Outline each blood parasite and name the species.
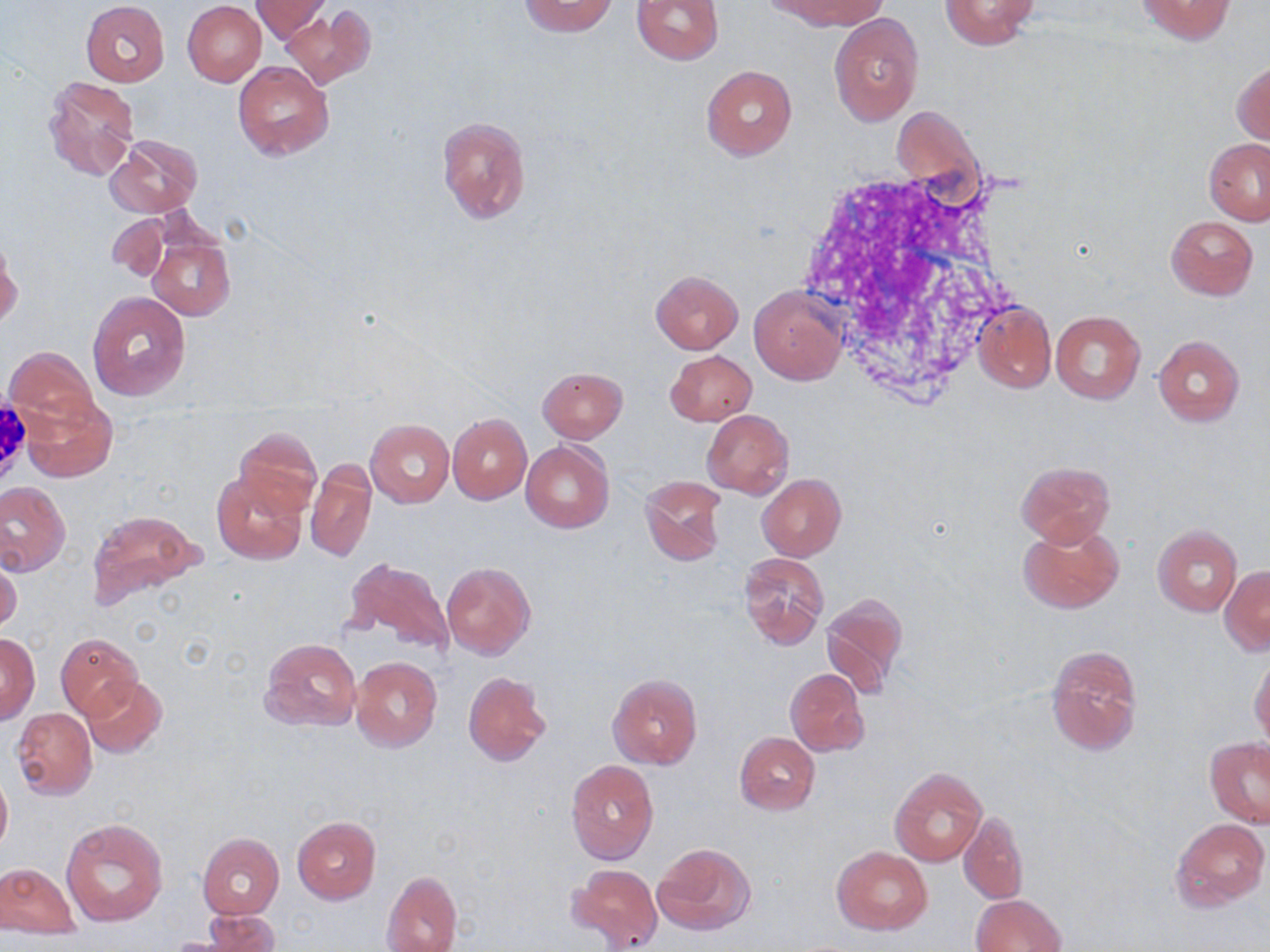

No blood parasites seen.

Approximate bounding boxes as named x1/y1/x2/y2 corners in pixels. Uninfected red blood cell locations: (x1=252, y1=0, x2=330, y2=43), (x1=518, y1=0, x2=617, y2=36), (x1=632, y1=0, x2=725, y2=65), (x1=772, y1=0, x2=885, y2=30), (x1=1133, y1=0, x2=1236, y2=44), (x1=81, y1=1, x2=169, y2=86), (x1=183, y1=1, x2=266, y2=86), (x1=938, y1=1, x2=1041, y2=49), (x1=281, y1=5, x2=375, y2=89), (x1=830, y1=13, x2=923, y2=125), (x1=1232, y1=60, x2=1270, y2=146), (x1=232, y1=61, x2=333, y2=161), (x1=701, y1=65, x2=795, y2=160), (x1=43, y1=75, x2=139, y2=183), (x1=436, y1=114, x2=531, y2=224), (x1=105, y1=134, x2=203, y2=220), (x1=1204, y1=138, x2=1270, y2=225), (x1=107, y1=214, x2=169, y2=281), (x1=1166, y1=215, x2=1258, y2=300), (x1=146, y1=228, x2=235, y2=321), (x1=1, y1=240, x2=21, y2=329), (x1=650, y1=270, x2=744, y2=353), (x1=750, y1=286, x2=846, y2=385), (x1=85, y1=290, x2=191, y2=401), (x1=973, y1=302, x2=1055, y2=393), (x1=1051, y1=310, x2=1145, y2=405), (x1=1153, y1=335, x2=1245, y2=426), (x1=4, y1=346, x2=102, y2=433), (x1=665, y1=350, x2=756, y2=425), (x1=536, y1=366, x2=628, y2=443), (x1=20, y1=390, x2=117, y2=482), (x1=702, y1=409, x2=794, y2=499), (x1=447, y1=413, x2=532, y2=504), (x1=365, y1=419, x2=454, y2=507), (x1=232, y1=427, x2=323, y2=519), (x1=521, y1=440, x2=615, y2=534), (x1=306, y1=459, x2=377, y2=564), (x1=1016, y1=460, x2=1116, y2=546), (x1=210, y1=470, x2=308, y2=565), (x1=756, y1=474, x2=846, y2=562), (x1=640, y1=475, x2=727, y2=566), (x1=0, y1=481, x2=71, y2=575), (x1=87, y1=510, x2=203, y2=610), (x1=1018, y1=520, x2=1124, y2=614), (x1=1152, y1=525, x2=1241, y2=616), (x1=738, y1=552, x2=828, y2=649), (x1=344, y1=556, x2=454, y2=657), (x1=0, y1=557, x2=22, y2=637), (x1=442, y1=561, x2=535, y2=659), (x1=1219, y1=566, x2=1270, y2=654), (x1=820, y1=593, x2=909, y2=697), (x1=1, y1=632, x2=39, y2=724), (x1=56, y1=633, x2=143, y2=720), (x1=259, y1=638, x2=361, y2=733), (x1=1046, y1=645, x2=1142, y2=754), (x1=350, y1=656, x2=443, y2=752), (x1=1249, y1=658, x2=1270, y2=744), (x1=785, y1=669, x2=868, y2=756), (x1=463, y1=671, x2=551, y2=766), (x1=608, y1=673, x2=702, y2=770), (x1=83, y1=677, x2=167, y2=758), (x1=11, y1=707, x2=96, y2=800), (x1=734, y1=732, x2=821, y2=815), (x1=1205, y1=737, x2=1268, y2=828), (x1=565, y1=761, x2=659, y2=864), (x1=890, y1=767, x2=987, y2=867), (x1=0, y1=769, x2=11, y2=855), (x1=959, y1=811, x2=1029, y2=905), (x1=293, y1=817, x2=380, y2=903), (x1=1170, y1=817, x2=1268, y2=913), (x1=61, y1=818, x2=169, y2=926), (x1=197, y1=833, x2=283, y2=918), (x1=652, y1=843, x2=755, y2=935), (x1=833, y1=848, x2=933, y2=935), (x1=0, y1=862, x2=79, y2=936), (x1=569, y1=863, x2=662, y2=950), (x1=382, y1=871, x2=463, y2=951), (x1=971, y1=893, x2=1067, y2=952), (x1=201, y1=909, x2=279, y2=952). Slide-level diagnosis: negative for blood parasites. Thin blood smear. May-Grünwald-Giemsa stain. Captured at 1000x magnification. Optical microscopy. One field of a larger specimen. Image is 1270×952 pixels.